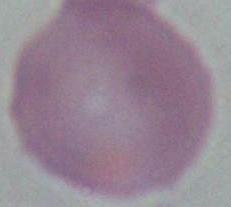
{
  "modality": "micrograph",
  "magnification": "1000x",
  "identification": "red blood cell"
}